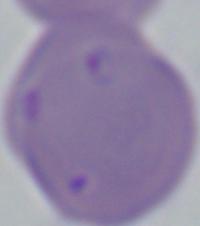
magnification = 1000x
modality = micrograph
identification = Babesia